Assess this cell for malaria.
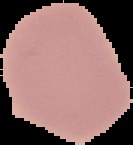

It is uninfected.

Cell region segmented out of the field of view; the surrounding area is masked to black. Image is 133×145 pixels. From a thin blood smear.